Assess this cell for malaria.
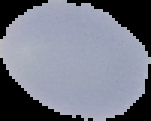

Uninfected.

Summary:
  - Image size: 151×121 pixels
  - Preparation: thin blood smear
  - Image type: segmented cell region with the area outside set to black